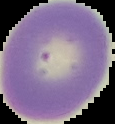
Summary:
  - Image size: 115×124 pixels
  - Malaria status: uninfected
  - Image type: segmented cell region with the area outside set to black
  - Preparation: thin blood smear